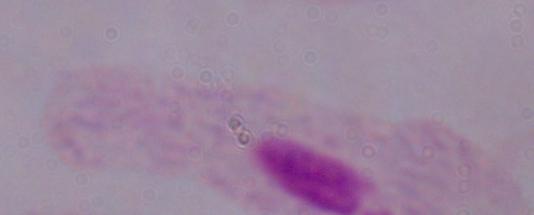 A trichomonad is seen. 1000x magnification. Micrograph.